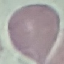

Result: no malaria parasites detected. Photographed with a smartphone camera at the microscope eyepiece. Automatically extracted cell patch, resized to 64 × 64 pixels. Thin smear of blood. Giemsa-stained preparation.